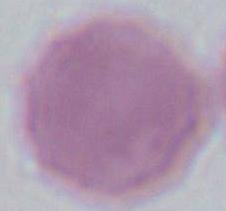
Summary:
  - Magnification: 1000x
  - Modality: photomicrograph
  - Identification: erythrocyte